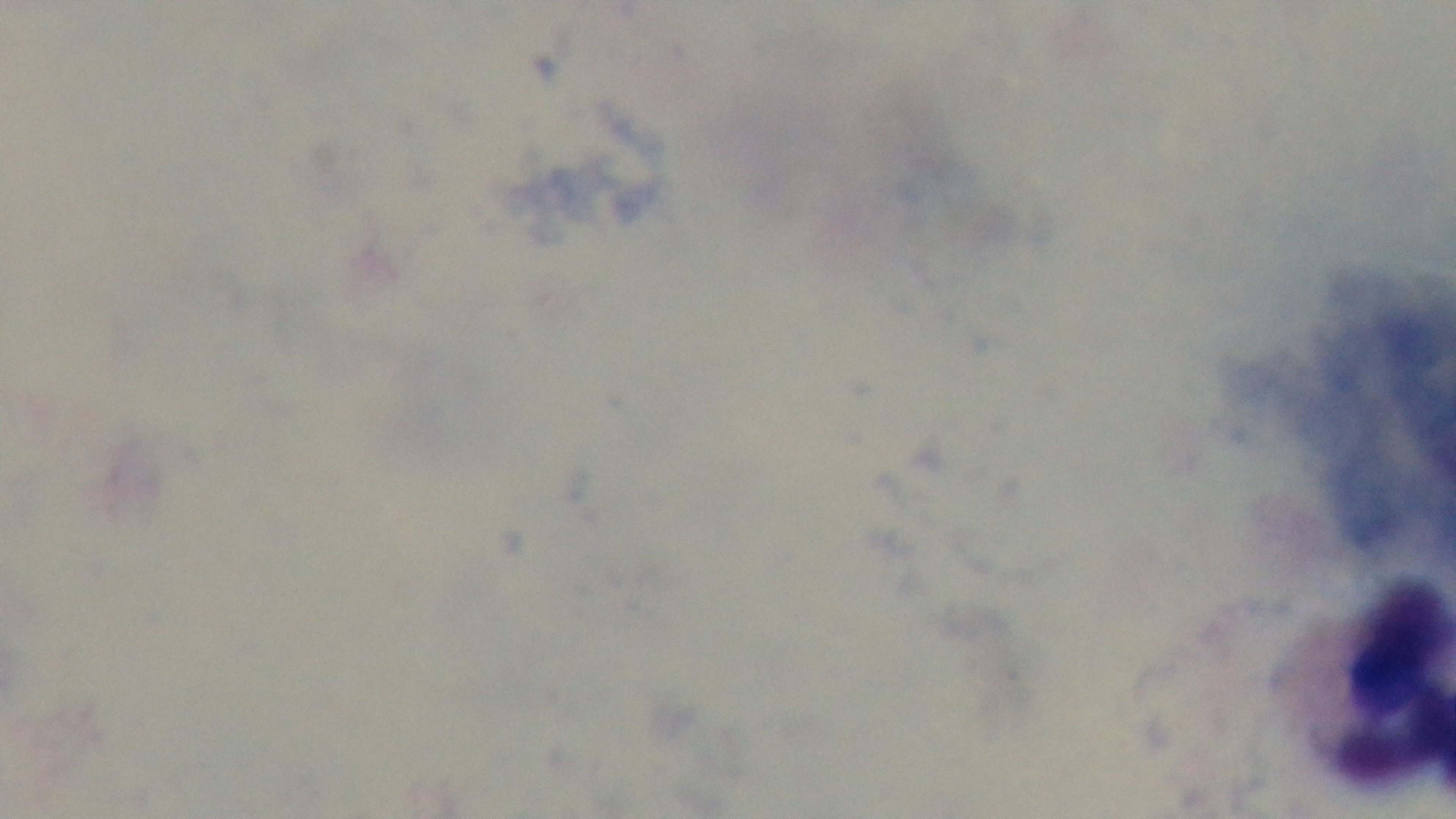
Malaria status: negative. Preparation: thick smear. Photomicrograph. Mounted 4K digital camera. Giemsa stain. Single field of view. Oil-immersion objective, 100x.